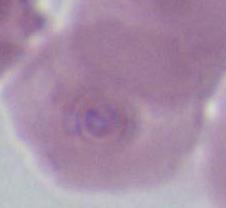

magnification = 1000x
identification = red blood cell
modality = photomicrograph